Classify this cell by malaria status.
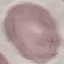

Uninfected.

{
  "stain": "Giemsa",
  "preparation": "thin smear",
  "image_type": "automatically extracted cell patch, resized to 64 × 64 pixels",
  "capture": "smartphone camera at the microscope eyepiece"
}